Identify the blood parasite species.
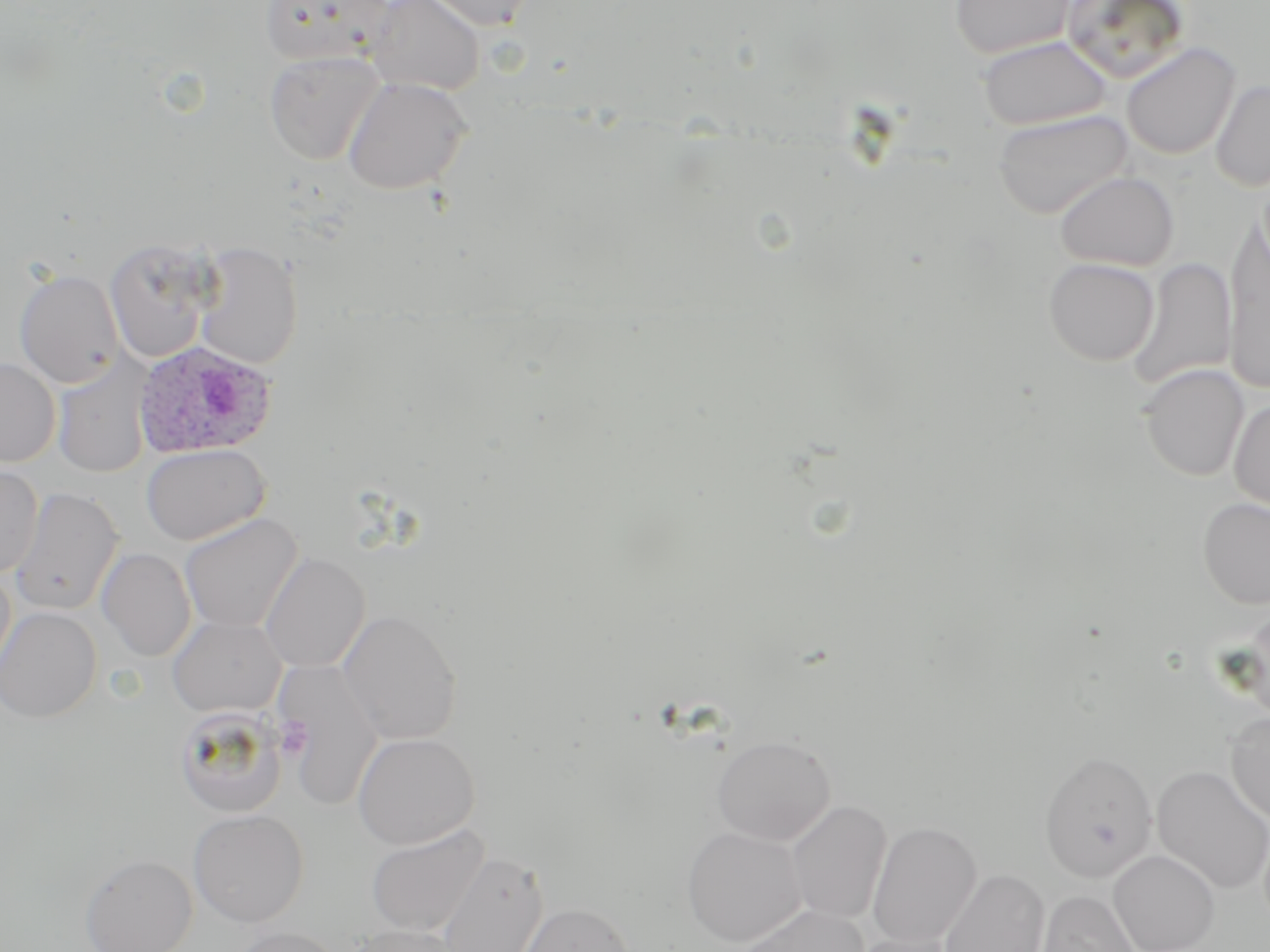

Plasmodium ovale.

Approximate bounding boxes as named x1/y1/x2/y2 corners in pixels. Platelet locations: (x1=275, y1=717, x2=312, y2=760). Plasmodium ovale-infected red blood cell locations: (x1=133, y1=340, x2=278, y2=459). Uninfected red blood cell locations: (x1=260, y1=0, x2=395, y2=68), (x1=364, y1=0, x2=485, y2=96), (x1=421, y1=0, x2=539, y2=31), (x1=948, y1=0, x2=1077, y2=60), (x1=1060, y1=0, x2=1191, y2=84), (x1=977, y1=35, x2=1113, y2=131), (x1=1121, y1=42, x2=1241, y2=160), (x1=264, y1=50, x2=385, y2=165), (x1=342, y1=76, x2=472, y2=195), (x1=1210, y1=79, x2=1270, y2=191), (x1=993, y1=109, x2=1134, y2=219), (x1=1053, y1=169, x2=1179, y2=271), (x1=1224, y1=225, x2=1270, y2=395), (x1=104, y1=239, x2=215, y2=363), (x1=193, y1=242, x2=303, y2=370), (x1=1127, y1=256, x2=1237, y2=392), (x1=1043, y1=258, x2=1159, y2=366), (x1=14, y1=269, x2=124, y2=388), (x1=0, y1=358, x2=61, y2=467), (x1=53, y1=361, x2=151, y2=478), (x1=1140, y1=364, x2=1249, y2=481), (x1=1230, y1=398, x2=1270, y2=512), (x1=140, y1=443, x2=270, y2=546), (x1=0, y1=463, x2=43, y2=577), (x1=9, y1=487, x2=123, y2=616), (x1=1198, y1=497, x2=1270, y2=608), (x1=179, y1=513, x2=302, y2=633), (x1=97, y1=547, x2=196, y2=662), (x1=260, y1=553, x2=370, y2=672), (x1=0, y1=564, x2=16, y2=683), (x1=0, y1=606, x2=101, y2=722), (x1=1237, y1=607, x2=1270, y2=724), (x1=338, y1=608, x2=462, y2=745), (x1=168, y1=616, x2=286, y2=717), (x1=276, y1=659, x2=384, y2=811), (x1=174, y1=705, x2=287, y2=817), (x1=1225, y1=712, x2=1270, y2=824), (x1=352, y1=732, x2=480, y2=849), (x1=712, y1=734, x2=835, y2=845), (x1=1046, y1=754, x2=1164, y2=886), (x1=1151, y1=764, x2=1270, y2=894), (x1=786, y1=799, x2=892, y2=925), (x1=189, y1=808, x2=309, y2=927), (x1=866, y1=821, x2=981, y2=948), (x1=365, y1=824, x2=491, y2=938), (x1=682, y1=826, x2=807, y2=946), (x1=1109, y1=849, x2=1220, y2=952), (x1=436, y1=851, x2=549, y2=952), (x1=80, y1=853, x2=198, y2=952), (x1=938, y1=868, x2=1050, y2=952), (x1=1037, y1=891, x2=1141, y2=952), (x1=519, y1=902, x2=634, y2=952), (x1=732, y1=904, x2=869, y2=952), (x1=342, y1=925, x2=466, y2=952), (x1=227, y1=926, x2=345, y2=952), (x1=848, y1=932, x2=962, y2=952). Thin blood smear. One field of a larger specimen. Image is 1270×952 pixels. May-Grünwald-Giemsa-stained preparation. Captured at 1000x magnification. Light microscopy.